Report the malaria status of this cell.
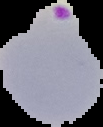
Parasitized.

Summary:
  - Preparation: thin blood film
  - Image size: 103×127 pixels
  - Image type: cell region segmented out of the field of view; surrounding area masked to black